Locate and identify every blood parasite.
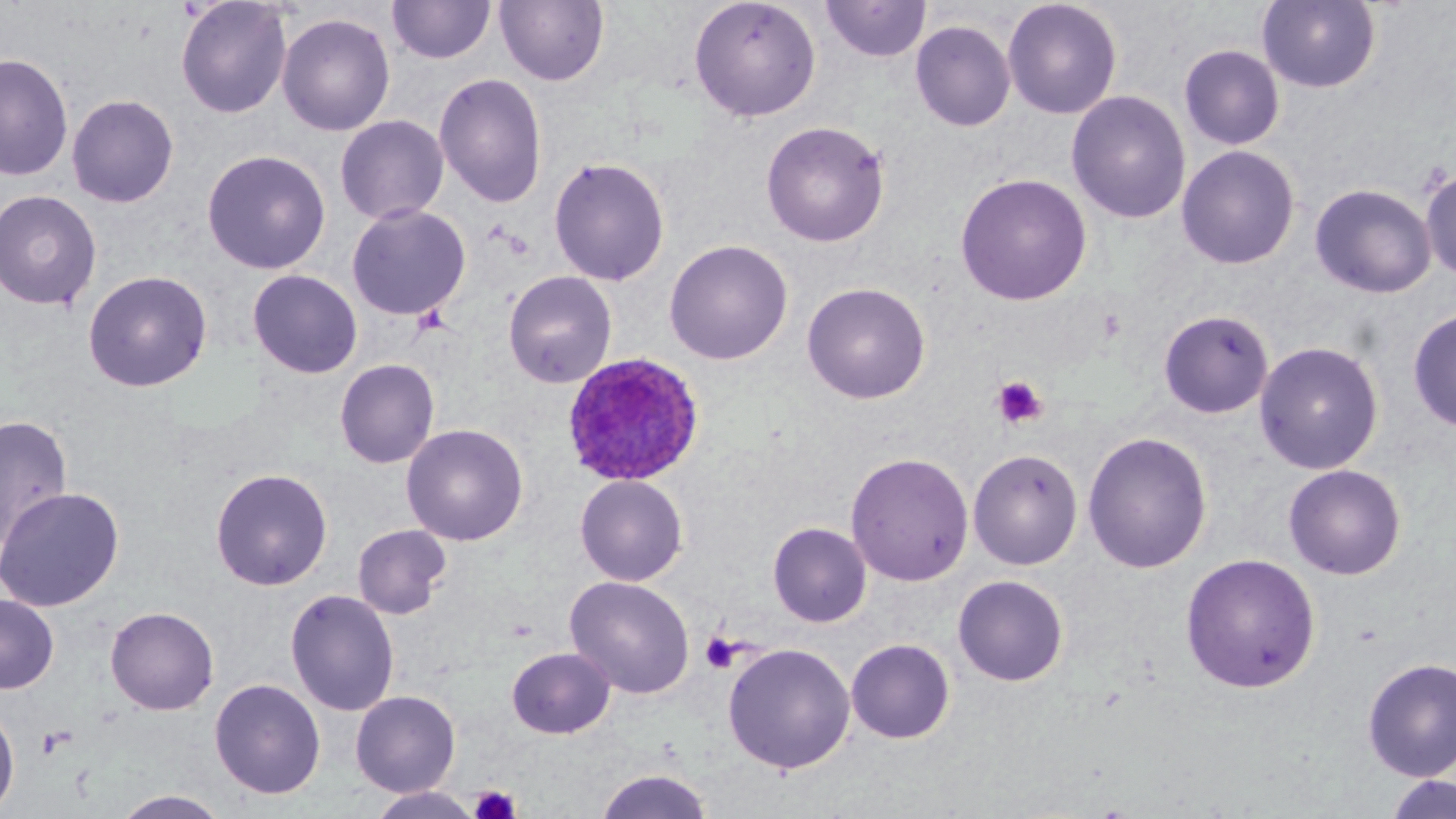

Approximate bounding boxes as (x1,y1)-(x2,y2) corner pairs in pixels.
Plasmodium ovale-infected red blood cells: (561,351)-(704,487).
No Plasmodium falciparum, Plasmodium malariae, Plasmodium vivax, Babesia divergens, or Trypanosoma brucei observed.

{
  "slide_level_diagnosis": "Plasmodium ovale",
  "platelet_locations": "approximate bounding boxes as (x1,y1)-(x2,y2) corner pairs in pixels: (991,375)-(1048,429), (700,633)-(739,674), (37,727)-(71,760), (469,784)-(522,819)",
  "image_size": "1456×819 pixels",
  "uninfected_red_blood_cell_locations": "approximate bounding boxes as (x1,y1)-(x2,y2) corner pairs in pixels: (175,0)-(293,119), (495,0)-(609,86), (688,0)-(821,122), (1002,0)-(1123,119), (1256,0)-(1382,93), (387,1)-(496,64), (820,1)-(931,63), (276,12)-(395,136), (910,20)-(1016,132), (1179,44)-(1285,150), (0,52)-(74,180), (434,72)-(547,208), (1066,90)-(1191,224), (66,93)-(179,208), (335,114)-(449,225), (761,120)-(890,247), (1176,145)-(1300,270), (202,149)-(331,275), (549,156)-(670,286), (1420,166)-(1456,282), (955,172)-(1092,306), (1309,183)-(1437,299), (0,189)-(102,310), (346,203)-(471,321), (664,239)-(793,365), (82,269)-(213,392), (247,269)-(363,379), (503,271)-(617,388), (802,281)-(931,404), (1407,308)-(1456,432), (1158,309)-(1273,419), (1254,341)-(1384,475), (334,359)-(440,469), (0,413)-(74,549), (401,423)-(529,545), (1082,431)-(1213,573), (968,448)-(1083,570), (845,452)-(973,586), (1283,463)-(1406,580), (210,467)-(333,591), (574,474)-(689,586), (0,487)-(124,612), (768,522)-(872,627), (352,524)-(451,619), (1180,553)-(1321,693), (953,575)-(1069,686), (565,576)-(695,699), (285,589)-(400,716), (0,593)-(59,694), (105,606)-(219,715), (846,638)-(955,744), (722,642)-(856,774), (506,646)-(616,739), (1362,657)-(1456,781), (209,678)-(326,799), (350,689)-(460,797), (0,701)-(20,815), (594,767)-(714,818), (1383,774)-(1456,819), (366,787)-(482,819), (113,789)-(230,818)",
  "preparation": "thin blood film",
  "stain": "May-Grünwald-Giemsa",
  "modality": "light microscopy",
  "field_of_view": "one of a larger specimen",
  "magnification": "1000x"
}